Point out each malaria parasite.
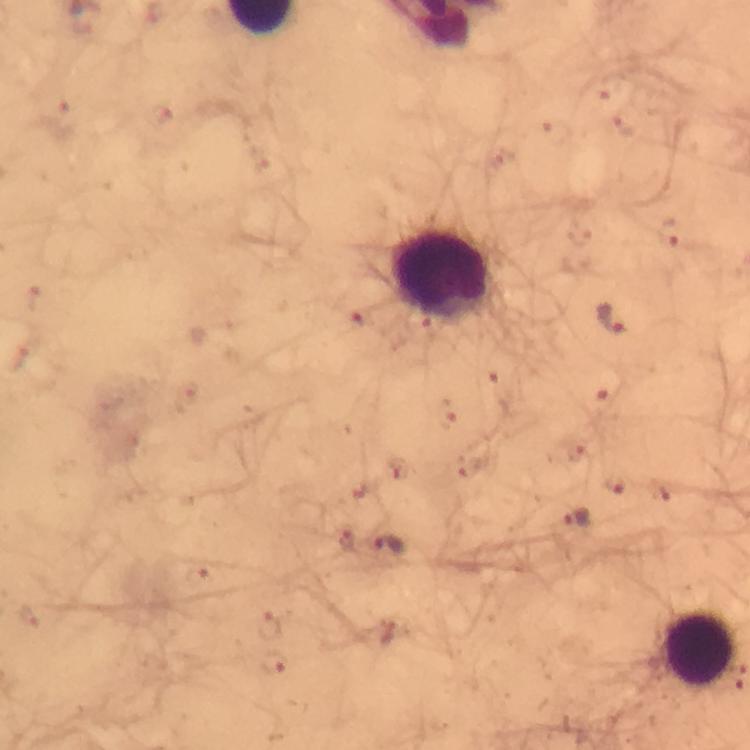
Approximate centers as [x, y] in pixels.
Malaria parasites: [611, 85], [158, 113], [61, 119], [625, 125], [557, 131], [673, 231], [34, 298], [610, 318], [358, 319], [19, 358], [498, 388], [602, 404], [446, 413], [570, 450], [615, 483], [575, 518], [343, 536], [389, 544], [196, 574], [27, 615], [270, 625], [389, 632], [274, 662].

Leukocyte locations: [444, 276], [699, 649]. Giemsa stain. From a malaria diagnostic workup. Immersion oil was used. Cropped region of a single field of view. At 100x magnification. Thick blood smear. Photographed with a smartphone mounted on the microscope. Image is 750×750 pixels.